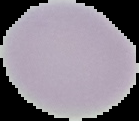
{
  "image_type": "cell region segmented out of the field of view; surrounding area masked to black",
  "malaria_status": "uninfected",
  "preparation": "thin blood film",
  "image_size": "139×121 pixels"
}